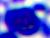
A leukocyte is shown. Photomicrograph. 400x magnification.